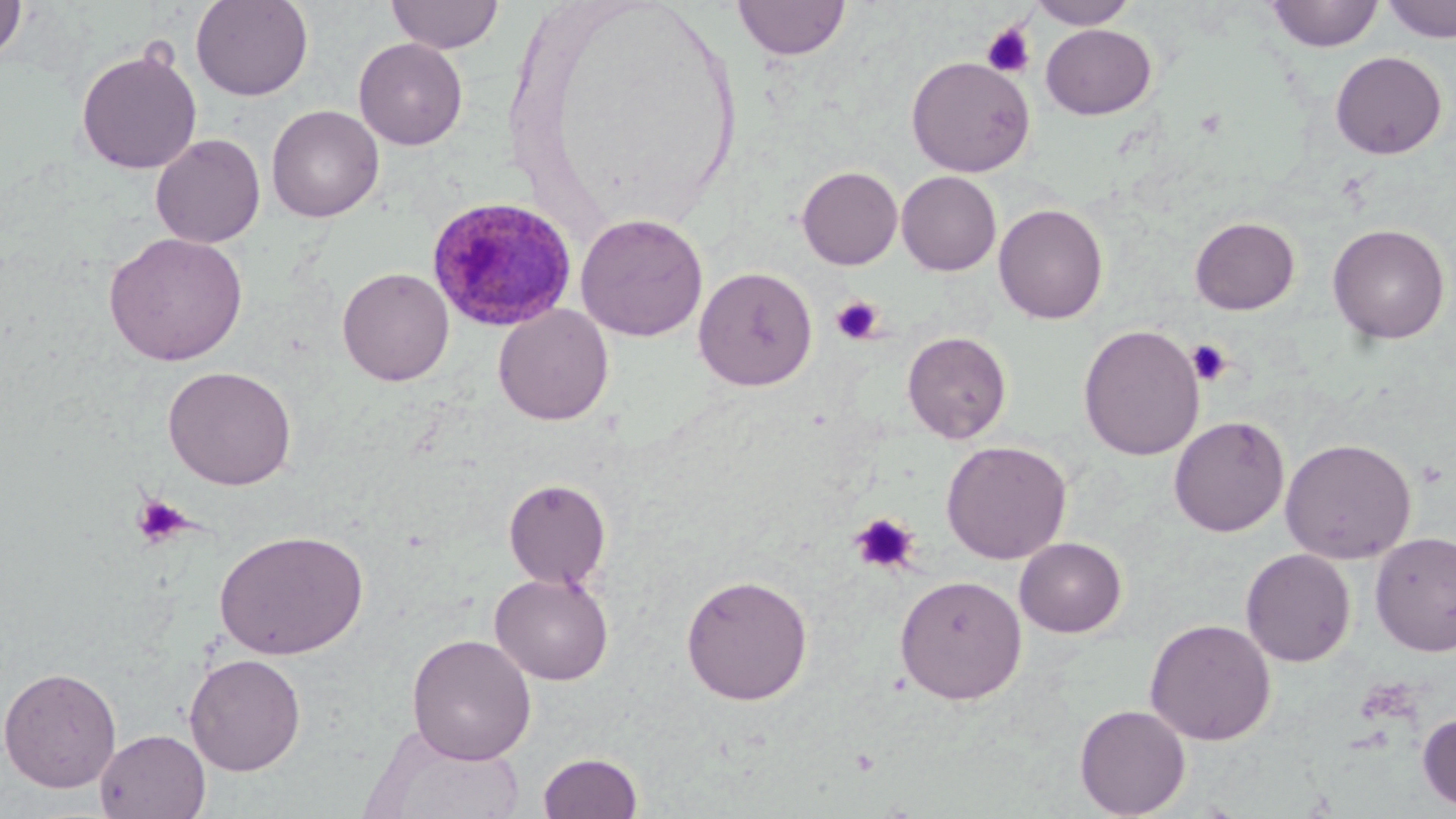

Summary:
  - Coordinate format: approximate bounding boxes as (x1, y1, x2, y2) in pixels
  - Uninfected red blood cell locations: (0, 0, 28, 65), (191, 0, 313, 101), (386, 0, 505, 54), (733, 0, 850, 60), (1027, 0, 1138, 29), (1267, 0, 1383, 51), (1383, 0, 1456, 43), (1040, 23, 1156, 119), (354, 38, 468, 149), (76, 46, 202, 175), (1329, 50, 1448, 159), (906, 55, 1035, 177), (266, 104, 384, 222), (151, 133, 266, 248), (796, 166, 903, 270), (896, 171, 1002, 275), (993, 202, 1109, 324), (575, 212, 708, 341), (1189, 216, 1300, 315), (1327, 223, 1450, 344), (104, 231, 248, 366), (693, 265, 818, 391), (337, 267, 454, 385), (493, 304, 614, 425), (1078, 324, 1204, 461), (902, 330, 1012, 443), (163, 365, 297, 490), (1168, 415, 1290, 536), (1280, 438, 1417, 563), (941, 440, 1072, 564), (503, 478, 612, 590), (214, 529, 367, 660), (1370, 531, 1456, 656), (1014, 537, 1127, 638), (1240, 548, 1356, 667), (490, 572, 614, 685), (680, 572, 813, 705), (894, 573, 1027, 704), (1144, 618, 1276, 745), (406, 633, 537, 764), (184, 653, 306, 775), (0, 665, 122, 792), (1074, 704, 1191, 818), (1417, 712, 1456, 813), (95, 729, 211, 818), (373, 732, 529, 819), (537, 750, 643, 818)
  - Platelet locations: (980, 21, 1036, 79), (829, 295, 885, 345), (1187, 339, 1233, 387), (132, 493, 191, 547), (849, 513, 920, 575)
  - Plasmodium ovale-infected red blood cell locations: (426, 195, 578, 331)
  - Slide-level diagnosis: Plasmodium ovale
  - Preparation: thin blood film
  - Image size: 1456×819 pixels
  - Stain: May-Grünwald-Giemsa
  - Magnification: 1000x
  - Field of view: one of a larger specimen
  - Modality: optical microscopy